State which parasite is depicted.
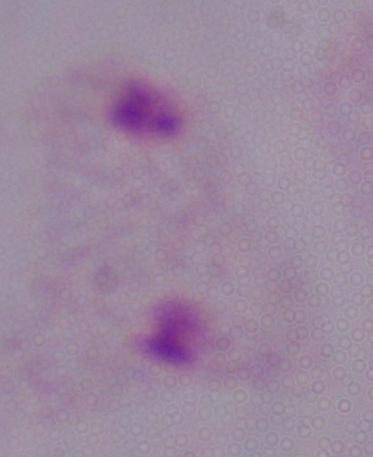

This is a trichomonad.

Captured at 1000x magnification. Micrograph.